Locate every parasitized red blood cell.
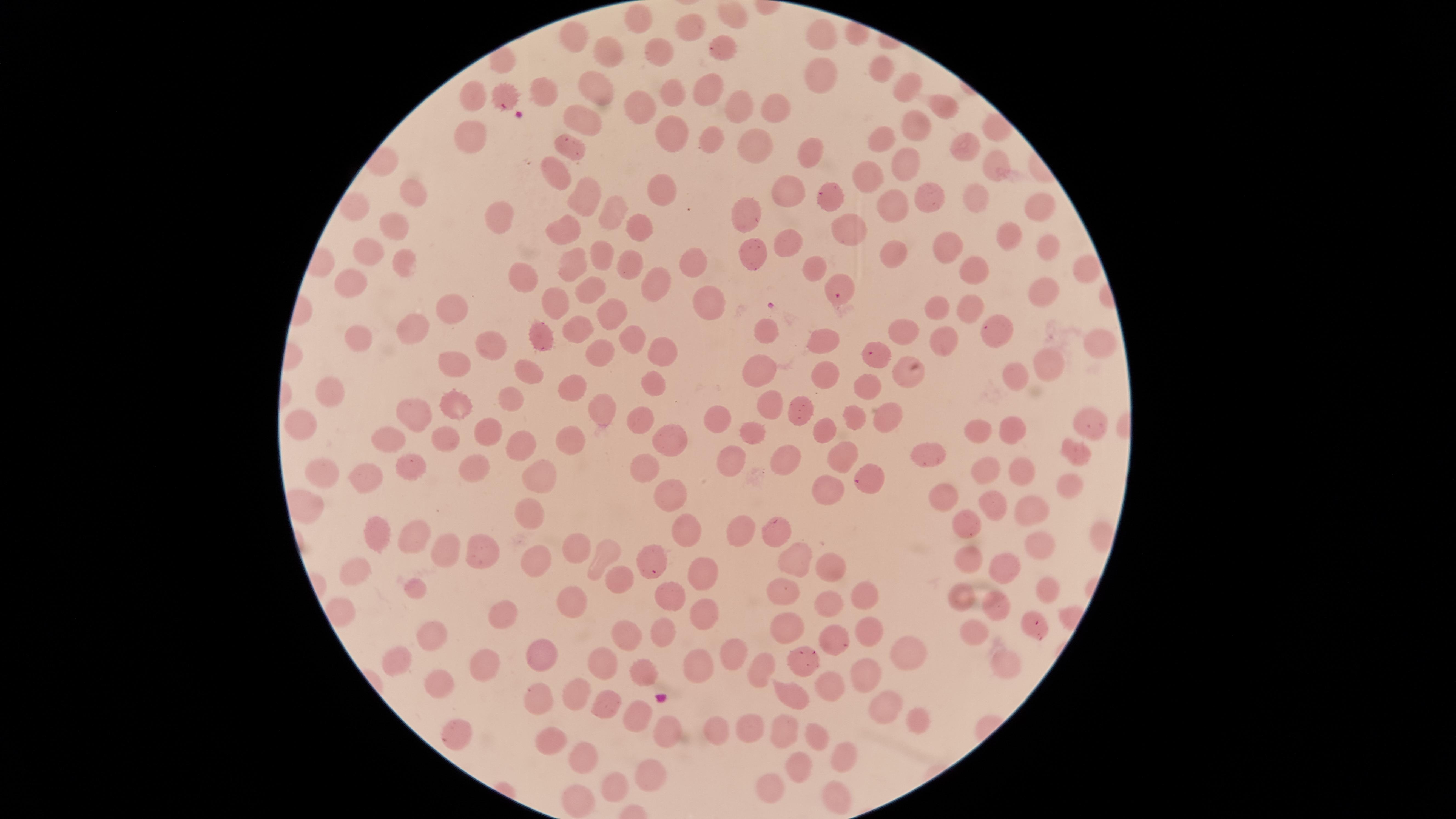
Approximate marker points, in pixels from the top-left corner.
Parasitized red blood cells: (x=502, y=102), (x=837, y=295), (x=653, y=572).

Approximate marker points, in pixels from the top-left corner.
Summary:
  - Uninfected red blood cells: (x=638, y=22), (x=687, y=29), (x=574, y=35), (x=823, y=39), (x=720, y=45), (x=606, y=51), (x=659, y=52), (x=881, y=71), (x=823, y=76), (x=596, y=87), (x=711, y=87), (x=906, y=87), (x=673, y=92), (x=473, y=95), (x=543, y=95), (x=736, y=101), (x=771, y=102), (x=943, y=105), (x=641, y=108), (x=579, y=119), (x=913, y=120), (x=672, y=133), (x=475, y=136), (x=712, y=140), (x=760, y=141), (x=881, y=142), (x=964, y=144), (x=571, y=147), (x=812, y=151), (x=904, y=163), (x=997, y=164), (x=559, y=170), (x=873, y=176), (x=792, y=188), (x=665, y=190), (x=409, y=191), (x=926, y=195), (x=582, y=196), (x=973, y=196), (x=1038, y=203), (x=834, y=205), (x=891, y=205), (x=355, y=208), (x=750, y=212), (x=611, y=214), (x=501, y=217), (x=391, y=224), (x=638, y=226), (x=567, y=228), (x=850, y=228), (x=1013, y=233), (x=788, y=237), (x=1046, y=245), (x=952, y=248), (x=371, y=255), (x=895, y=255), (x=752, y=256), (x=605, y=257), (x=692, y=258), (x=405, y=260), (x=572, y=262), (x=629, y=262), (x=815, y=267), (x=971, y=267), (x=1083, y=270), (x=527, y=278), (x=655, y=281), (x=352, y=285), (x=1044, y=289), (x=589, y=292), (x=711, y=302), (x=554, y=305), (x=969, y=305), (x=937, y=306), (x=615, y=311), (x=446, y=312), (x=905, y=328), (x=414, y=330), (x=765, y=331), (x=580, y=332), (x=544, y=333), (x=632, y=334), (x=939, y=337), (x=993, y=337), (x=361, y=338), (x=824, y=338), (x=1096, y=339), (x=488, y=345), (x=665, y=345), (x=599, y=351), (x=880, y=361), (x=1051, y=361), (x=762, y=364), (x=455, y=368), (x=533, y=373), (x=828, y=373), (x=1016, y=374), (x=913, y=377), (x=656, y=386), (x=569, y=387), (x=869, y=387), (x=329, y=392), (x=511, y=399), (x=457, y=406), (x=600, y=406), (x=763, y=406), (x=790, y=410), (x=422, y=414), (x=855, y=415), (x=888, y=417), (x=1084, y=418), (x=644, y=420), (x=303, y=421), (x=714, y=421), (x=827, y=429), (x=484, y=431), (x=1010, y=435), (x=392, y=436), (x=750, y=437), (x=445, y=439), (x=671, y=439), (x=976, y=439), (x=565, y=440), (x=526, y=441), (x=1073, y=450), (x=728, y=454), (x=782, y=455), (x=841, y=457), (x=932, y=458), (x=413, y=464), (x=646, y=467), (x=473, y=471), (x=324, y=473), (x=1016, y=475), (x=371, y=476), (x=979, y=476), (x=866, y=477), (x=534, y=478), (x=1065, y=485), (x=831, y=492), (x=668, y=494), (x=944, y=497), (x=991, y=501), (x=1033, y=506), (x=529, y=512), (x=968, y=524), (x=736, y=530), (x=773, y=530), (x=381, y=534), (x=412, y=535), (x=686, y=535), (x=1039, y=544), (x=568, y=546), (x=448, y=549), (x=482, y=551), (x=601, y=553), (x=968, y=556), (x=790, y=558), (x=533, y=560), (x=1001, y=564), (x=826, y=567), (x=355, y=573), (x=697, y=574), (x=619, y=577), (x=414, y=587), (x=1048, y=588), (x=785, y=592), (x=862, y=595), (x=667, y=598), (x=961, y=598), (x=991, y=603), (x=569, y=605), (x=831, y=605), (x=499, y=608), (x=703, y=611), (x=787, y=628), (x=866, y=628), (x=1039, y=628), (x=621, y=630), (x=663, y=631), (x=976, y=633), (x=435, y=634), (x=832, y=638), (x=395, y=651), (x=906, y=651), (x=540, y=656), (x=730, y=657), (x=485, y=662), (x=601, y=662), (x=1008, y=663), (x=695, y=666), (x=799, y=666), (x=765, y=667), (x=644, y=675), (x=867, y=675), (x=446, y=683), (x=826, y=684), (x=790, y=688), (x=572, y=691), (x=540, y=701), (x=600, y=704), (x=884, y=708), (x=637, y=712), (x=917, y=714), (x=749, y=725), (x=713, y=729), (x=778, y=731), (x=662, y=732), (x=457, y=733), (x=813, y=736), (x=546, y=737), (x=580, y=756), (x=845, y=761), (x=646, y=768), (x=792, y=768), (x=769, y=789), (x=615, y=790), (x=834, y=796), (x=584, y=806)
  - Capture: smartphone photograph through the microscope eyepiece
  - Stain: Giemsa
  - Field of view: single
  - Image size: 1456×819 pixels
  - Visible region: circular
  - Preparation: thin blood film
  - Species: Plasmodium falciparum